Give the position of every Plasmodium parasite.
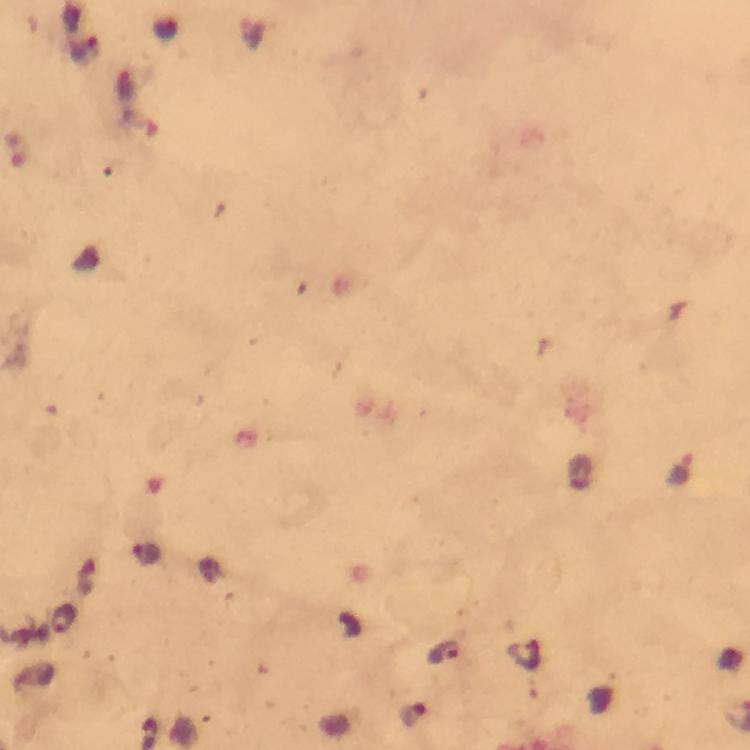
Approximate centers as (x, y) in pixels.
Plasmodium parasites: (681, 472), (145, 554), (63, 619), (444, 654), (412, 714).

Image is 750×750 pixels. Smartphone photograph taken through a microscope. At 100x magnification. From a diagnostic examination for malaria. Cropped region of a single field of view. Giemsa stain. Immersion oil was used. Thick smear.